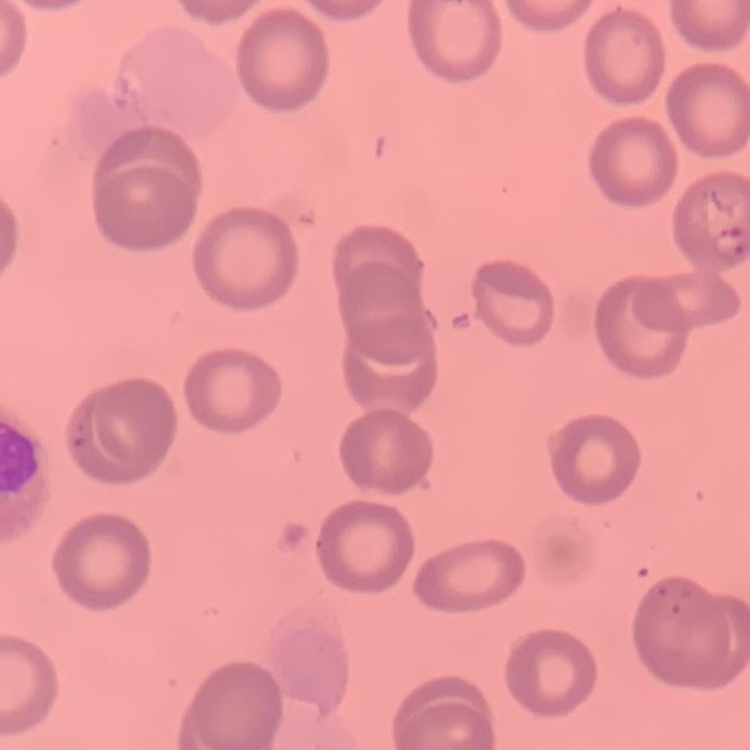
Summary:
  - Erythrocyte morphology: no rouleaux formation
  - Image type: square crop of a larger photomicrograph
  - Preparation: thin peripheral smear
  - Stain: Field's or Giemsa